Locate every Plasmodium malariae-infected red blood cell.
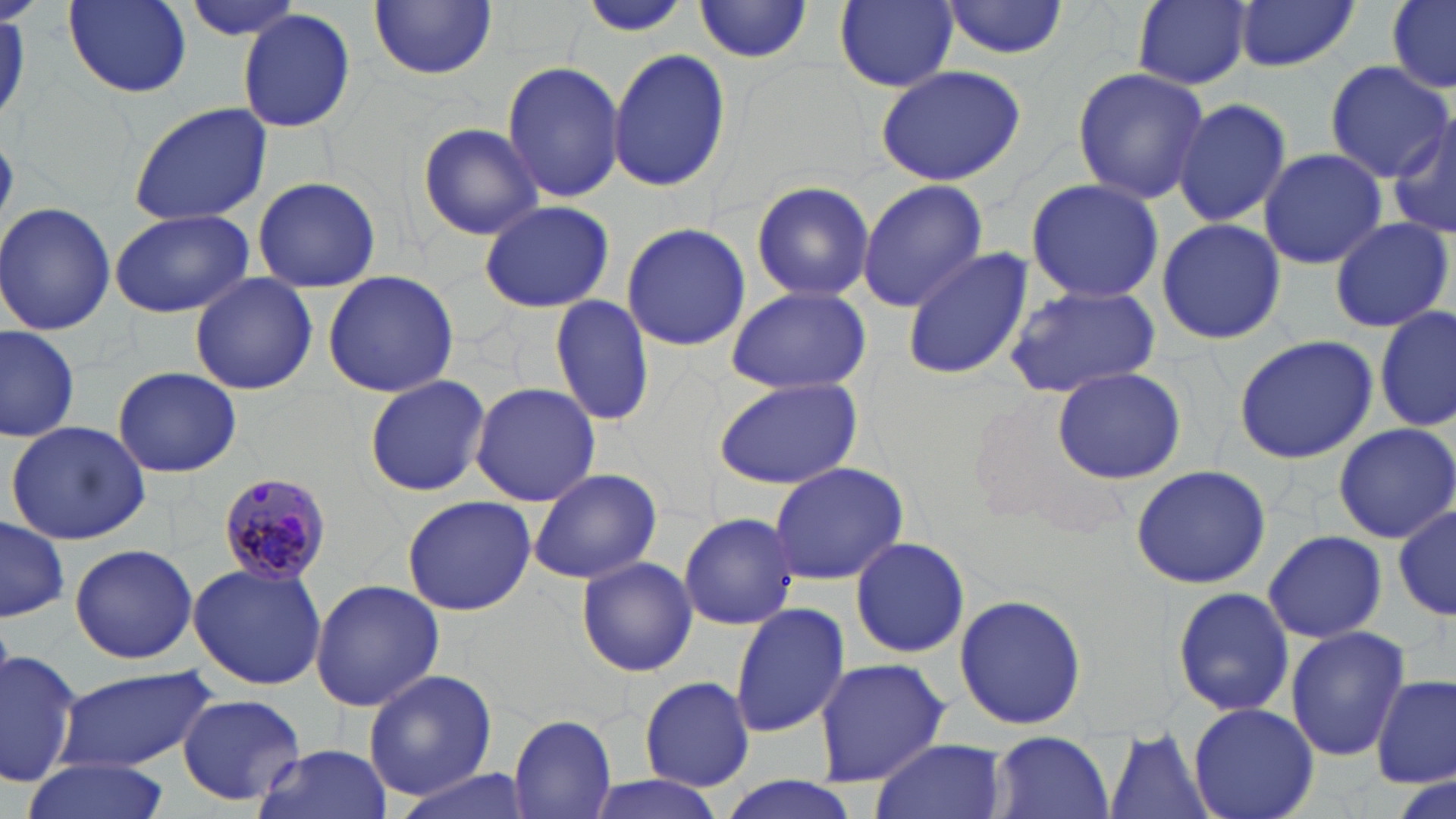
Approximate bounding boxes as [x1, y1, x2, y2] in pixels.
Plasmodium malariae-infected red blood cells: [218, 472, 334, 584].

Uninfected red blood cell locations: [64, 0, 193, 97], [178, 0, 309, 42], [1133, 0, 1254, 90], [1232, 0, 1360, 73], [1389, 0, 1456, 91], [835, 1, 959, 90], [941, 1, 1070, 59], [370, 2, 498, 80], [577, 2, 689, 38], [693, 2, 815, 65], [237, 9, 358, 134], [607, 47, 731, 193], [501, 59, 625, 204], [1323, 63, 1450, 179], [876, 64, 1028, 187], [1070, 66, 1209, 204], [1172, 100, 1293, 230], [127, 102, 274, 225], [1386, 113, 1456, 245], [416, 122, 543, 241], [1257, 147, 1388, 270], [252, 175, 382, 294], [856, 179, 988, 312], [1025, 179, 1166, 303], [752, 180, 876, 304], [478, 199, 615, 312], [0, 202, 117, 336], [110, 209, 256, 318], [1156, 216, 1286, 347], [1328, 216, 1454, 334], [621, 222, 751, 353], [900, 246, 1032, 382], [321, 270, 460, 397], [190, 272, 316, 395], [1004, 284, 1165, 400], [723, 285, 873, 394], [549, 294, 656, 427], [1375, 306, 1455, 431], [0, 326, 79, 444], [1231, 334, 1378, 465], [112, 365, 243, 479], [1051, 365, 1189, 483], [365, 374, 490, 495], [712, 376, 864, 489], [469, 382, 599, 506], [5, 418, 154, 545], [1333, 424, 1455, 541], [768, 461, 911, 584], [1131, 464, 1272, 590], [527, 467, 664, 585], [401, 495, 537, 616], [1389, 499, 1456, 626], [678, 512, 801, 631], [0, 519, 70, 622], [1263, 530, 1386, 643], [848, 535, 971, 659], [70, 542, 197, 665], [576, 556, 698, 678], [188, 562, 329, 690], [309, 579, 443, 713], [1171, 585, 1295, 720], [952, 593, 1090, 732], [730, 603, 850, 737], [1283, 625, 1411, 762], [0, 645, 86, 788], [812, 659, 948, 786], [57, 667, 218, 772], [361, 667, 498, 800], [1374, 676, 1454, 789], [640, 677, 755, 791], [178, 693, 305, 806], [1188, 702, 1318, 819], [508, 715, 617, 819], [1105, 730, 1213, 818], [988, 731, 1115, 819], [870, 737, 1006, 819], [252, 742, 392, 819], [22, 758, 171, 819], [390, 767, 536, 819], [582, 775, 732, 819], [707, 777, 869, 819]. Slide-level diagnosis: Plasmodium malariae. One field of a larger specimen. Thin blood smear. Image is 1456×819 pixels. 1000x magnification. May-Grünwald-Giemsa-stained preparation. Light microscopy.